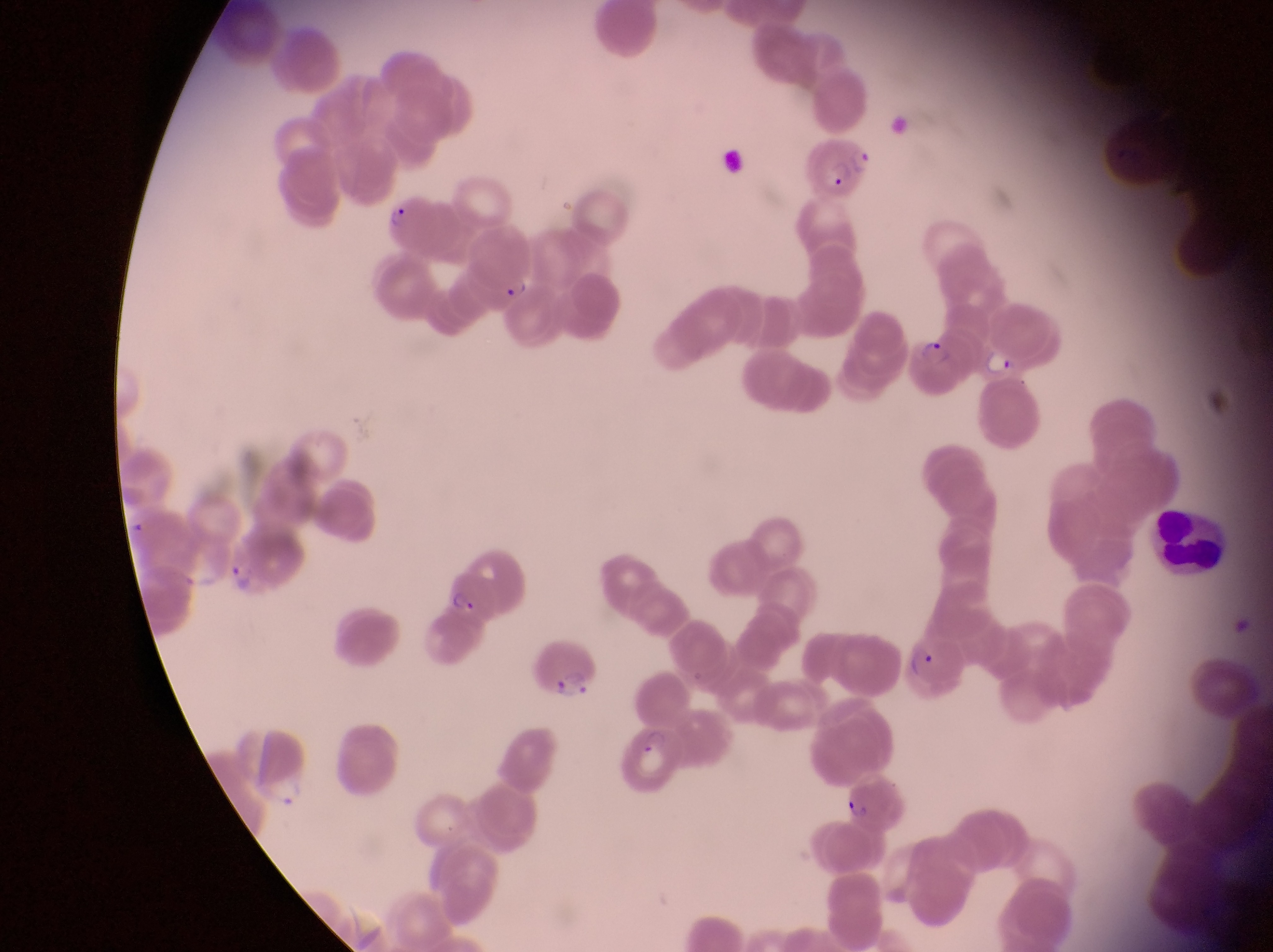

Approximate bounding boxes as left top right bottom in pixels.
Summary:
  - Parasitised red blood cell locations: 804 134 879 201; 377 190 435 255; 464 220 544 303; 911 332 971 399; 440 565 497 618; 535 635 604 702; 906 635 969 700; 836 774 911 837
  - Leukocyte locations: 1152 501 1226 581
  - Trophozoite locations: 984 346 1017 380; 226 554 260 593
  - Field of view: single
  - Country: Uganda
  - Capture: smartphone photograph through the eyepiece of an Olympus CX-23 microscope
  - Image size: 1273×952 pixels
  - Preparation: thin blood smear
  - Magnification: 1000x